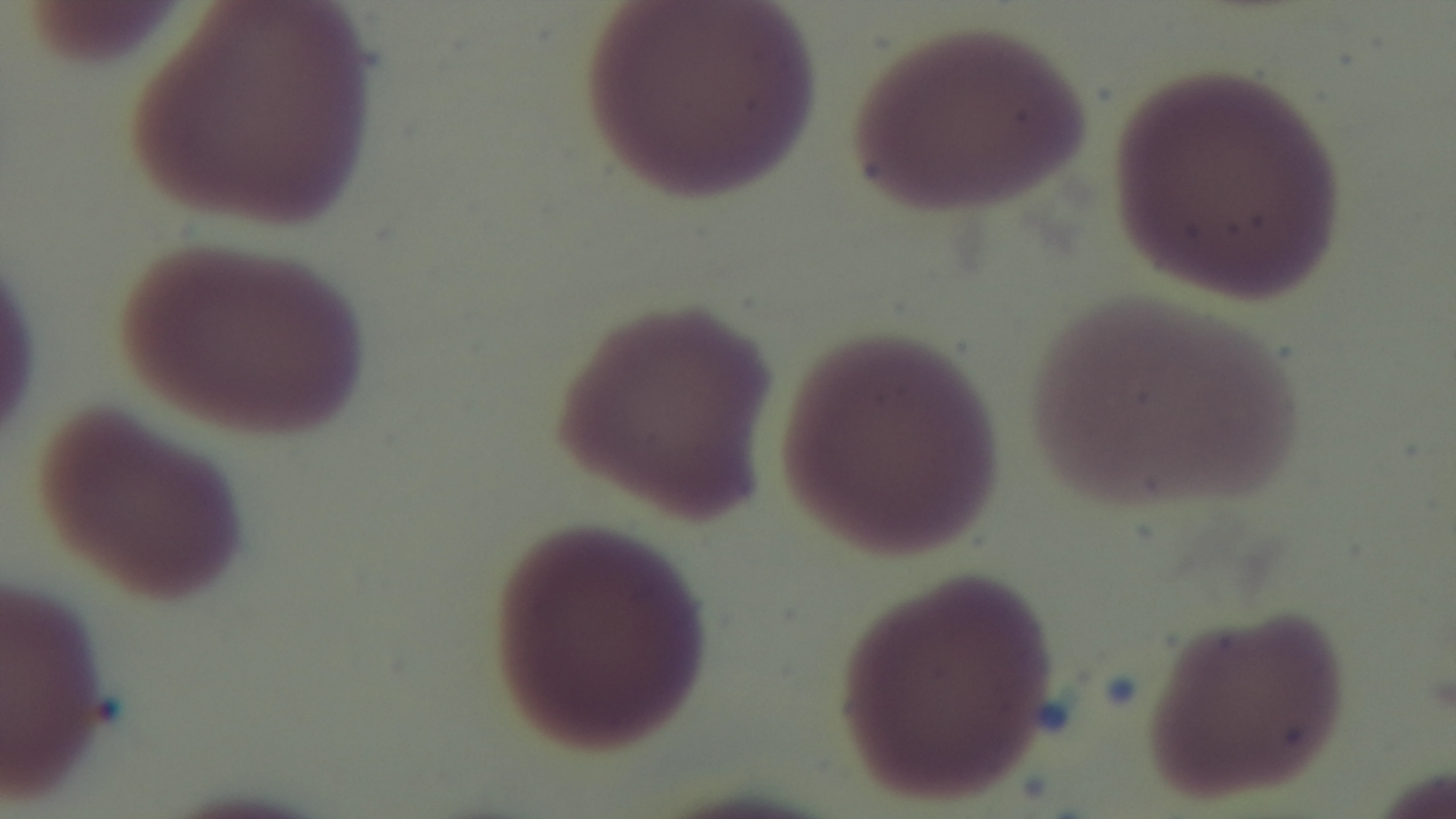

Summary:
  - Malaria status: uninfected
  - Preparation: thin blood film
  - Objective: 100x oil immersion
  - Field of view: one from the slide
  - Capture: mounted 4K digital camera
  - Modality: light microscopy
  - Stain: Giemsa